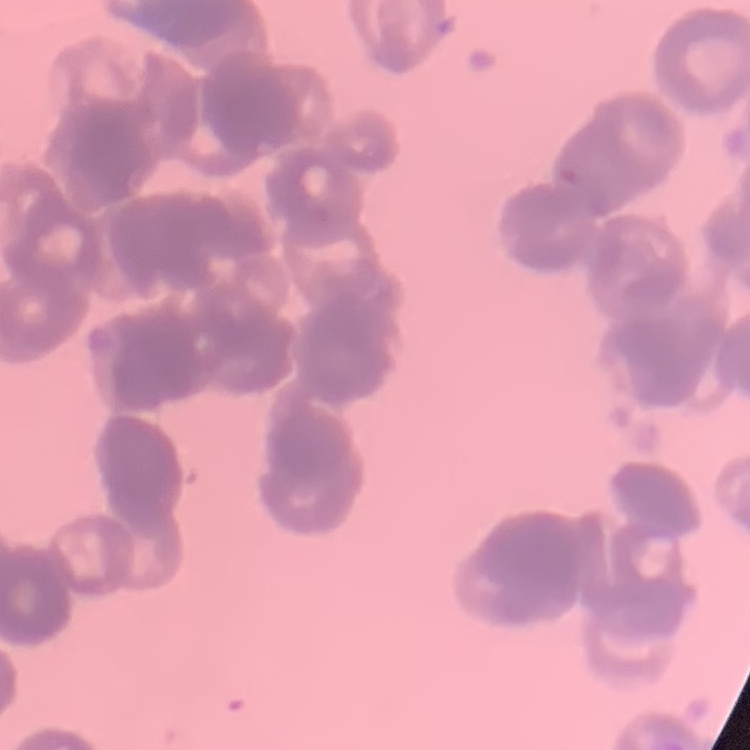

{
  "red_blood_cell_morphology": "rouleaux formation",
  "preparation": "thin blood smear",
  "image_type": "square crop of a larger photomicrograph",
  "stain": "Field's or Giemsa"
}